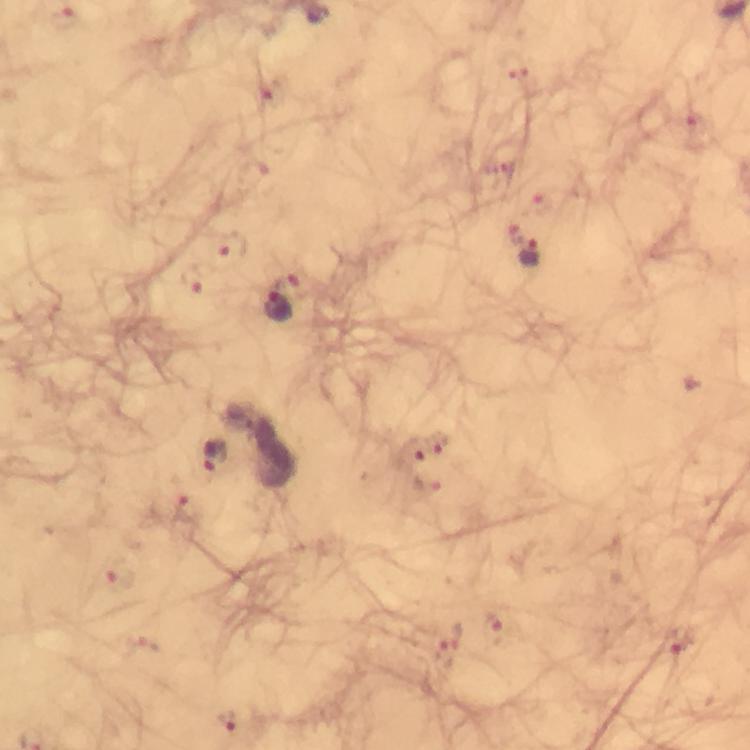

magnification: 100x
capture: smartphone mounted on the microscope
preparation: thick smear
immersion_oil: used
malaria_parasite_locations: 'approximate centers as (x, y) in pixels: (66, 19), (515, 66), (270, 94), (698, 126), (500, 170), (253, 175), (541, 204), (515, 232), (231, 245), (531, 253), (192, 280), (279, 309), (440, 444), (412, 451), (216, 454), (426, 486), (187, 509), (120, 578), (493, 627), (679, 638), (147, 643), (445, 655), (229, 720)'
cropped_from: one field of view
stain: Giemsa
image_size: 750×750 pixels
context: from a diagnostic examination for malaria